Assess this cell for malaria.
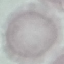
Uninfected.

Thin smear of blood. Giemsa-stained preparation. Photographed with a smartphone camera at the microscope eyepiece. Automatically extracted cell patch, resized to 64 × 64 pixels.